Name the blood parasite species.
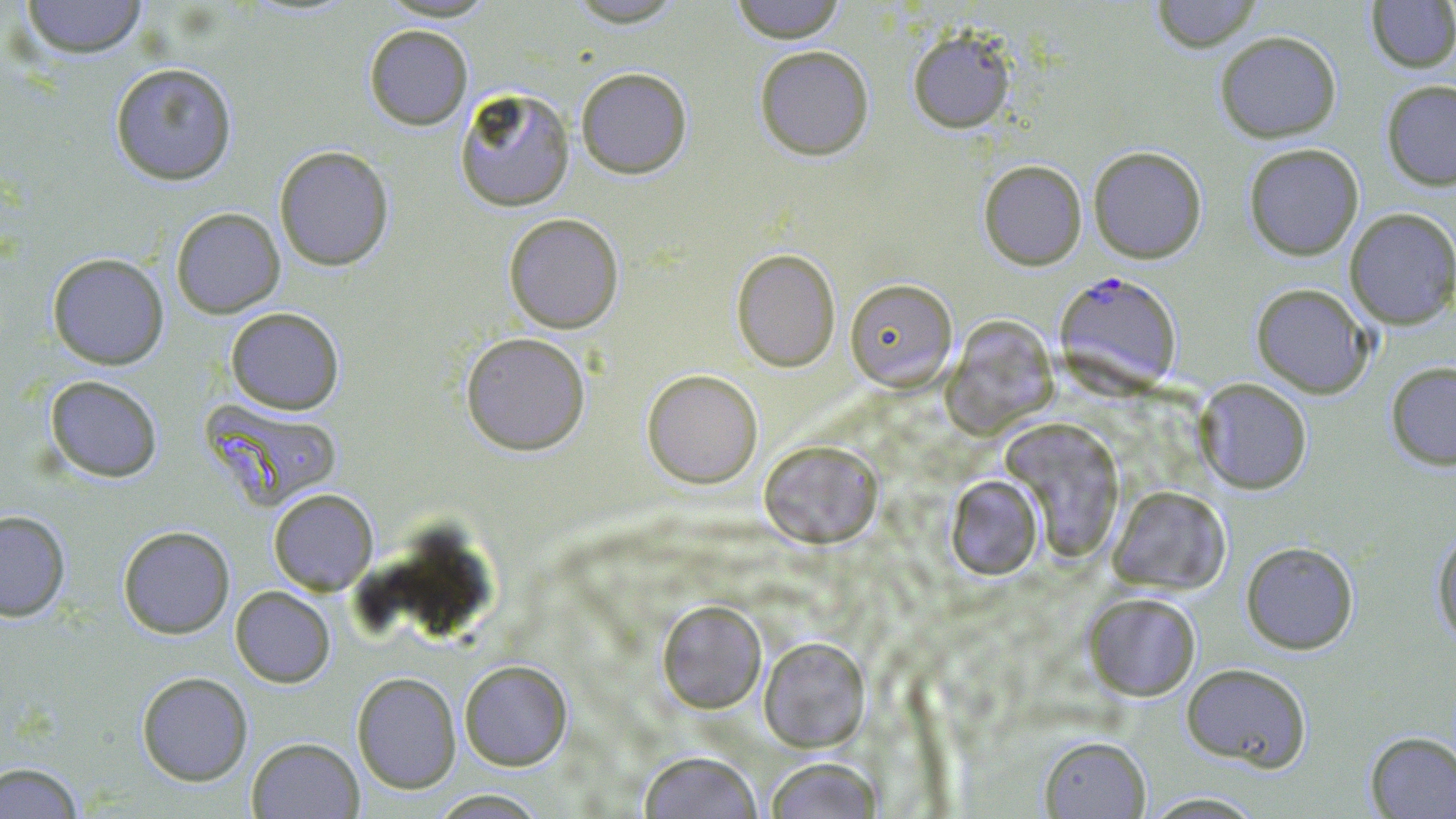
Plasmodium falciparum.

{
  "stain": "May-Grünwald-Giemsa",
  "modality": "light microscopy",
  "magnification": "1000x",
  "field_of_view": "single",
  "image_size": "1456×819 pixels",
  "preparation": "thin blood film",
  "uninfected_red_blood_cell_locations": "approximate bounding boxes as named x1/y1/x2/y2 corners in pixels: (x1=20, y1=0, x2=148, y2=59), (x1=728, y1=0, x2=847, y2=43), (x1=1150, y1=0, x2=1262, y2=52), (x1=1366, y1=1, x2=1456, y2=72), (x1=364, y1=24, x2=473, y2=130), (x1=907, y1=26, x2=1017, y2=133), (x1=1215, y1=30, x2=1342, y2=142), (x1=754, y1=45, x2=874, y2=161), (x1=109, y1=62, x2=238, y2=185), (x1=575, y1=67, x2=692, y2=178), (x1=1381, y1=79, x2=1456, y2=191), (x1=454, y1=87, x2=575, y2=211), (x1=1243, y1=143, x2=1364, y2=260), (x1=274, y1=145, x2=394, y2=271), (x1=1088, y1=145, x2=1206, y2=264), (x1=978, y1=159, x2=1087, y2=270), (x1=171, y1=207, x2=285, y2=318), (x1=1344, y1=207, x2=1456, y2=329), (x1=503, y1=212, x2=624, y2=333), (x1=731, y1=248, x2=841, y2=371), (x1=47, y1=252, x2=169, y2=370), (x1=845, y1=278, x2=957, y2=391), (x1=1251, y1=283, x2=1373, y2=398), (x1=225, y1=307, x2=345, y2=415), (x1=944, y1=316, x2=1057, y2=434), (x1=460, y1=331, x2=591, y2=455), (x1=1385, y1=361, x2=1456, y2=470), (x1=642, y1=369, x2=763, y2=488), (x1=44, y1=375, x2=163, y2=482), (x1=1194, y1=378, x2=1312, y2=494), (x1=201, y1=399, x2=342, y2=511), (x1=1001, y1=419, x2=1126, y2=561), (x1=759, y1=439, x2=883, y2=548), (x1=945, y1=474, x2=1043, y2=580), (x1=1107, y1=485, x2=1230, y2=595), (x1=268, y1=488, x2=378, y2=595), (x1=0, y1=510, x2=70, y2=621), (x1=390, y1=523, x2=495, y2=641), (x1=118, y1=525, x2=235, y2=638), (x1=1432, y1=526, x2=1456, y2=646), (x1=1241, y1=541, x2=1359, y2=654), (x1=230, y1=586, x2=335, y2=687), (x1=1083, y1=591, x2=1201, y2=701), (x1=657, y1=600, x2=766, y2=713), (x1=759, y1=637, x2=870, y2=752), (x1=459, y1=660, x2=572, y2=771), (x1=1181, y1=662, x2=1312, y2=772), (x1=136, y1=671, x2=253, y2=786), (x1=352, y1=672, x2=461, y2=794), (x1=1365, y1=731, x2=1456, y2=818), (x1=1039, y1=735, x2=1150, y2=818), (x1=247, y1=737, x2=364, y2=818), (x1=638, y1=750, x2=763, y2=818), (x1=764, y1=757, x2=882, y2=819), (x1=0, y1=761, x2=84, y2=818), (x1=425, y1=789, x2=552, y2=818), (x1=1139, y1=791, x2=1270, y2=818)",
  "plasmodium_falciparum_infected_red_blood_cell_locations": "approximate bounding boxes as named x1/y1/x2/y2 corners in pixels: (x1=1055, y1=271, x2=1183, y2=395)"
}